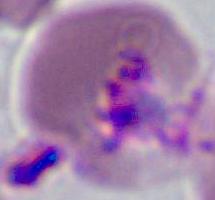
Summary:
  - Modality: micrograph
  - Magnification: 400x or 1000x
  - Identification: Plasmodium